State which parasite is depicted.
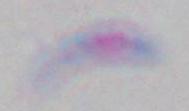
Toxoplasma gondii.

magnification: 1000x
modality: micrograph